Assess the morphology of the erythrocytes.
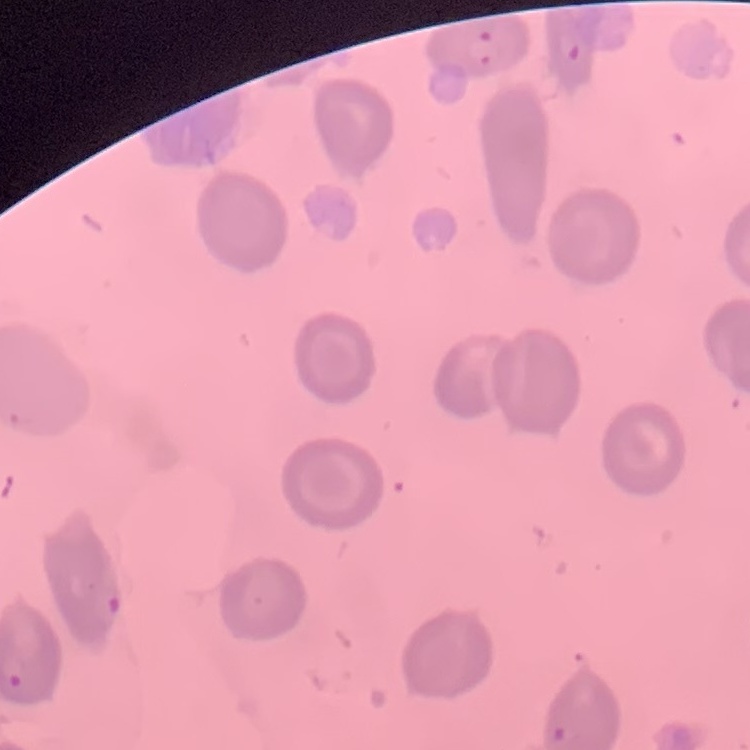
They show no rouleaux formation.

Thin peripheral smear. Field's or Giemsa stain. Square crop of a larger photomicrograph.